Describe the morphology of the erythrocytes.
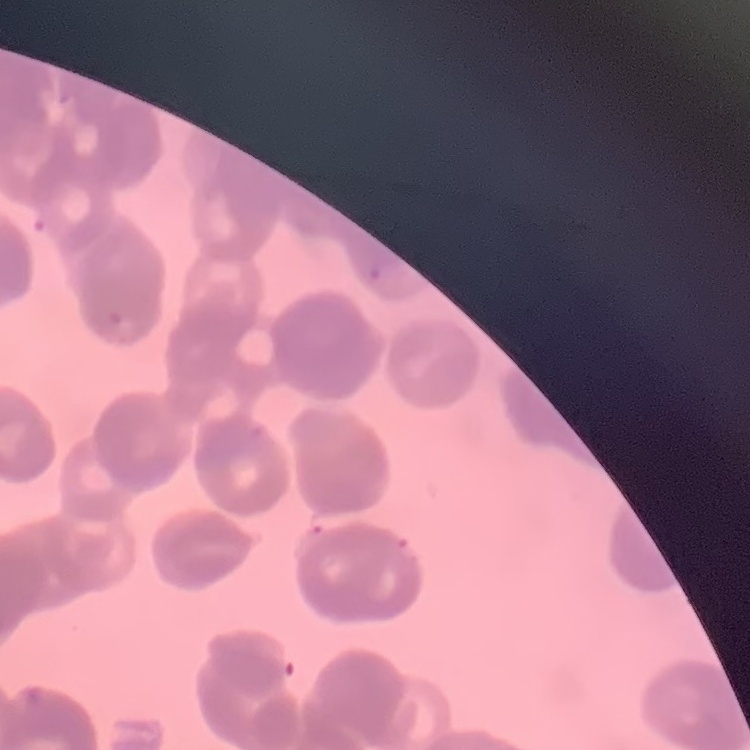

Rouleaux formation.

Summary:
  - Image type: square crop of a larger photomicrograph
  - Stain: Field's or Giemsa
  - Preparation: thin blood smear